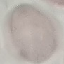
Summary:
  - Malaria status: uninfected
  - Stain: Giemsa
  - Preparation: thin blood smear
  - Image type: automatically extracted cell patch, resized to 64 × 64 pixels
  - Capture: smartphone camera at the microscope eyepiece